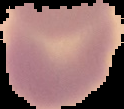
From a thin blood film. The area outside the segmented cell region is set to black. Result: no Plasmodium parasites detected. Image is 124×109 pixels.